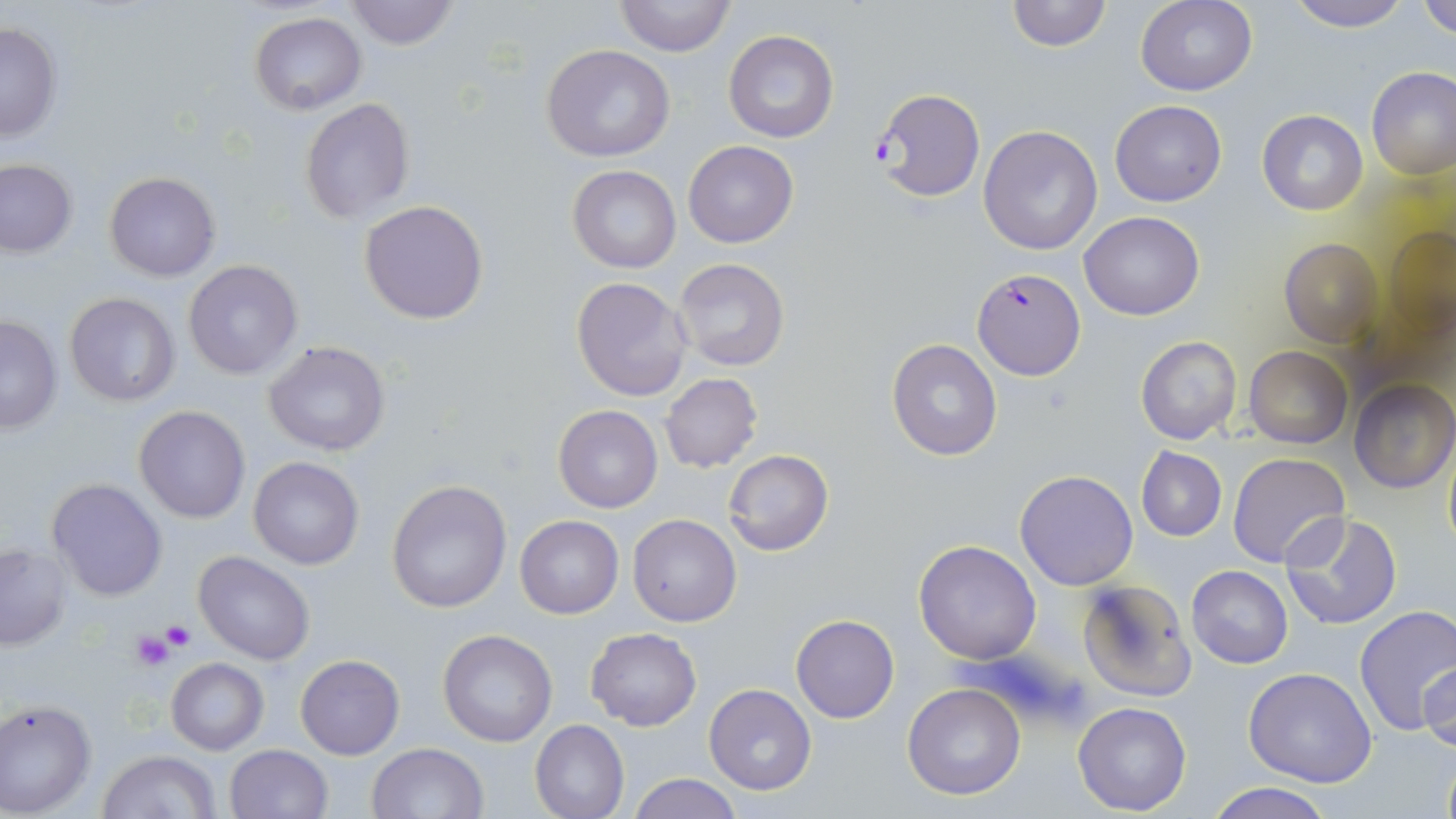

slide_level_diagnosis: Plasmodium falciparum
uninfected_red_blood_cell_locations: 'approximate bounding boxes as named x1/y1/x2/y2 corners in pixels: (x1=343, y1=0, x2=460, y2=49), (x1=612, y1=0, x2=736, y2=56), (x1=1005, y1=0, x2=1111, y2=51), (x1=1135, y1=0, x2=1258, y2=97), (x1=1287, y1=0, x2=1410, y2=31), (x1=1418, y1=0, x2=1456, y2=40), (x1=250, y1=11, x2=366, y2=114), (x1=0, y1=21, x2=62, y2=141), (x1=723, y1=29, x2=841, y2=145), (x1=540, y1=45, x2=677, y2=163), (x1=1367, y1=67, x2=1456, y2=180), (x1=299, y1=99, x2=414, y2=223), (x1=1110, y1=100, x2=1227, y2=206), (x1=1257, y1=109, x2=1368, y2=216), (x1=978, y1=125, x2=1103, y2=255), (x1=683, y1=140, x2=799, y2=249), (x1=0, y1=159, x2=77, y2=258), (x1=567, y1=164, x2=681, y2=273), (x1=103, y1=172, x2=220, y2=280), (x1=358, y1=200, x2=489, y2=324), (x1=1079, y1=212, x2=1204, y2=321), (x1=1377, y1=223, x2=1456, y2=344), (x1=1280, y1=238, x2=1385, y2=347), (x1=673, y1=256, x2=791, y2=373), (x1=183, y1=260, x2=304, y2=381), (x1=571, y1=276, x2=691, y2=400), (x1=63, y1=292, x2=181, y2=409), (x1=0, y1=315, x2=63, y2=433), (x1=1135, y1=334, x2=1243, y2=446), (x1=886, y1=338, x2=1002, y2=461), (x1=263, y1=341, x2=391, y2=456), (x1=1244, y1=346, x2=1352, y2=448), (x1=659, y1=373, x2=764, y2=473), (x1=1351, y1=379, x2=1456, y2=494), (x1=553, y1=404, x2=663, y2=513), (x1=133, y1=405, x2=251, y2=525), (x1=1443, y1=438, x2=1456, y2=558), (x1=1136, y1=446, x2=1228, y2=541), (x1=723, y1=449, x2=834, y2=556), (x1=1226, y1=453, x2=1349, y2=571), (x1=247, y1=457, x2=365, y2=570), (x1=1014, y1=470, x2=1140, y2=591), (x1=46, y1=478, x2=168, y2=602), (x1=385, y1=479, x2=512, y2=614), (x1=1279, y1=512, x2=1404, y2=630), (x1=628, y1=514, x2=742, y2=626), (x1=515, y1=515, x2=623, y2=619), (x1=912, y1=539, x2=1042, y2=665), (x1=0, y1=543, x2=72, y2=652), (x1=193, y1=549, x2=315, y2=665), (x1=1187, y1=566, x2=1293, y2=668), (x1=1077, y1=578, x2=1196, y2=703), (x1=1353, y1=605, x2=1456, y2=739), (x1=790, y1=614, x2=899, y2=723), (x1=586, y1=627, x2=702, y2=731), (x1=437, y1=629, x2=559, y2=747), (x1=295, y1=654, x2=404, y2=759), (x1=165, y1=657, x2=268, y2=755), (x1=1420, y1=660, x2=1455, y2=757), (x1=1244, y1=667, x2=1378, y2=787), (x1=902, y1=681, x2=1028, y2=801), (x1=703, y1=684, x2=817, y2=797), (x1=0, y1=698, x2=98, y2=816), (x1=1073, y1=702, x2=1191, y2=816), (x1=530, y1=719, x2=629, y2=819), (x1=368, y1=742, x2=489, y2=819), (x1=223, y1=744, x2=332, y2=819), (x1=1439, y1=747, x2=1456, y2=819), (x1=98, y1=750, x2=220, y2=819), (x1=628, y1=774, x2=744, y2=819), (x1=1205, y1=781, x2=1334, y2=819)'
image_size: 1456×819 pixels
stain: May-Grünwald-Giemsa
field_of_view: one of a larger specimen
platelet_locations: 'approximate bounding boxes as named x1/y1/x2/y2 corners in pixels: (x1=162, y1=620, x2=195, y2=650), (x1=129, y1=630, x2=174, y2=672)'
preparation: thin blood film
plasmodium_falciparum_infected_red_blood_cell_locations: 'approximate bounding boxes as named x1/y1/x2/y2 corners in pixels: (x1=871, y1=89, x2=986, y2=203), (x1=972, y1=267, x2=1087, y2=380)'
modality: optical microscopy
magnification: 1000x